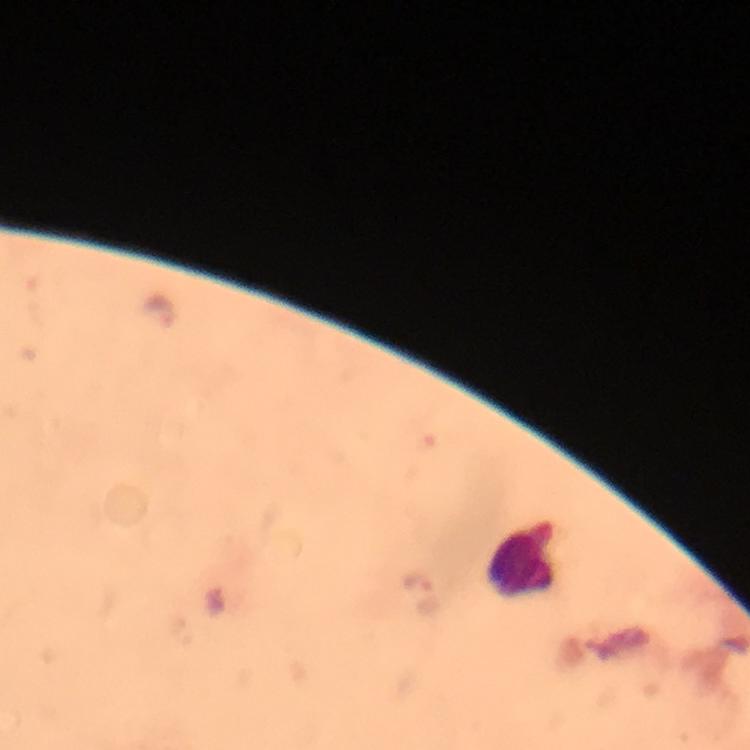

Approximate centers as [x, y] in pixels. Leukocyte locations: [522, 553]. Malaria parasite locations: [159, 313], [416, 584]. Giemsa stain. From a diagnostic examination for malaria. 100x magnification. Thick smear. Smartphone photograph taken through a microscope. Cropped region of a single field of view. Immersion oil applied. Image is 750×750 pixels.